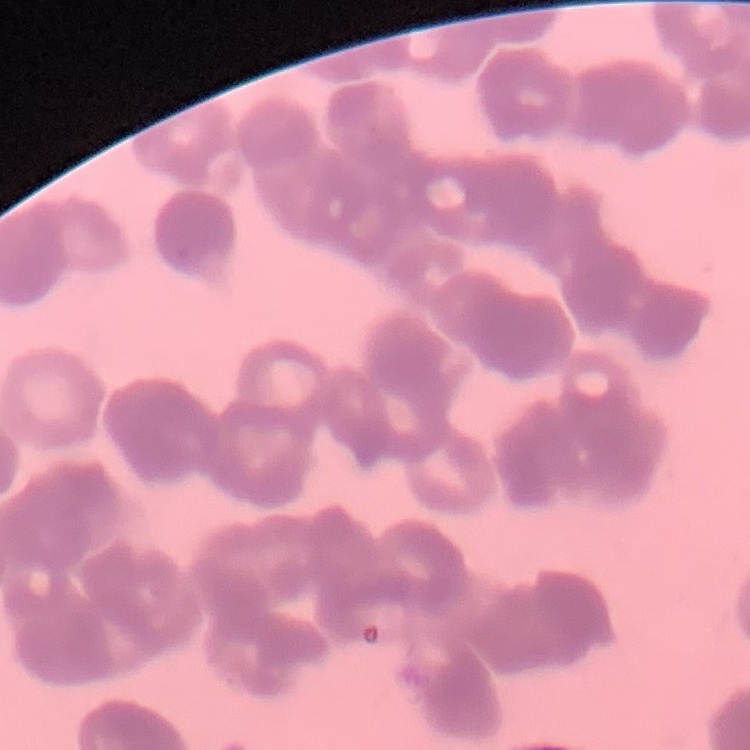
erythrocyte morphology = rouleaux formation
preparation = thin blood film
image type = square crop of a larger photomicrograph
stain = Field's or Giemsa